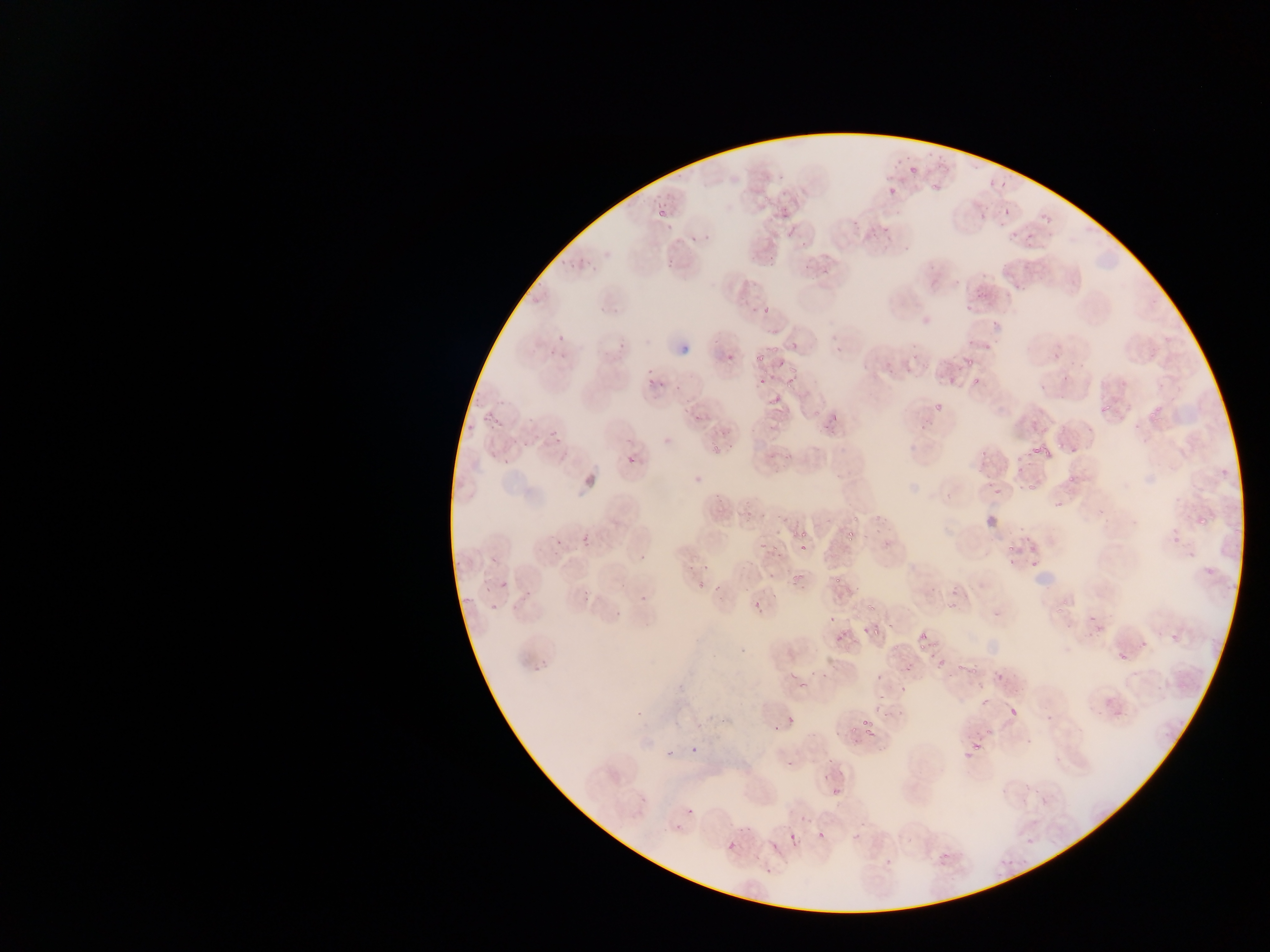
Approximate bounding boxes as [left, top, right, bottom] in pixels. Plasmodium parasite locations: [985, 149, 1012, 190], [905, 159, 918, 176], [932, 171, 947, 194], [887, 173, 905, 202], [1000, 201, 1012, 224], [774, 208, 782, 220], [1020, 211, 1044, 241], [663, 212, 681, 232], [686, 223, 703, 247], [663, 248, 680, 267], [1014, 261, 1022, 271], [820, 262, 843, 288], [969, 278, 989, 304], [758, 295, 781, 317], [986, 323, 1006, 334], [558, 329, 570, 344], [612, 340, 632, 352], [751, 349, 768, 364], [960, 349, 985, 366], [722, 354, 732, 364], [778, 357, 798, 375], [640, 364, 657, 376], [962, 368, 978, 391], [761, 373, 778, 387], [782, 373, 802, 397], [643, 379, 654, 390], [660, 384, 677, 395], [769, 392, 788, 411], [923, 397, 947, 416], [822, 406, 843, 432], [484, 407, 499, 433], [547, 422, 561, 437], [976, 434, 996, 472], [1027, 435, 1056, 458], [554, 436, 569, 450], [486, 451, 500, 466], [499, 452, 517, 469], [627, 453, 638, 464], [984, 462, 999, 484], [691, 470, 705, 484], [1022, 479, 1038, 493], [993, 480, 1004, 496], [1196, 500, 1207, 527], [582, 523, 596, 545], [842, 527, 858, 547], [552, 530, 569, 551], [797, 540, 811, 554], [1001, 543, 1016, 560], [640, 550, 646, 564], [1007, 557, 1019, 571], [700, 560, 718, 574], [1023, 561, 1040, 572], [685, 564, 693, 576], [792, 571, 808, 587], [494, 575, 512, 597], [578, 582, 593, 604], [639, 592, 647, 602], [752, 600, 760, 612], [613, 611, 621, 618], [1086, 618, 1103, 636], [868, 623, 884, 643], [832, 624, 848, 642], [1129, 630, 1155, 644], [1115, 633, 1139, 664], [918, 635, 929, 647], [935, 654, 948, 668], [1005, 703, 1024, 725], [858, 712, 878, 739], [791, 713, 803, 732], [770, 724, 778, 735], [966, 733, 991, 758], [683, 744, 699, 758], [661, 751, 671, 762], [782, 754, 790, 768], [828, 777, 851, 806], [685, 806, 696, 817], [814, 828, 831, 850], [788, 829, 804, 846], [726, 842, 738, 854], [767, 842, 781, 853], [938, 849, 956, 871], [765, 861, 785, 876] | approximate [x, y] pixel centers of objects too small to bound: [551, 355]. Mobile-phone photograph taken through the microscope. Single field of view. Thin blood smear. Sample from Ghana. Image is 1270×952 pixels.